Identify the parasite.
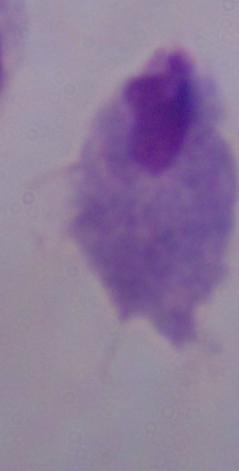
A trichomonad.

1000x magnification. Micrograph.